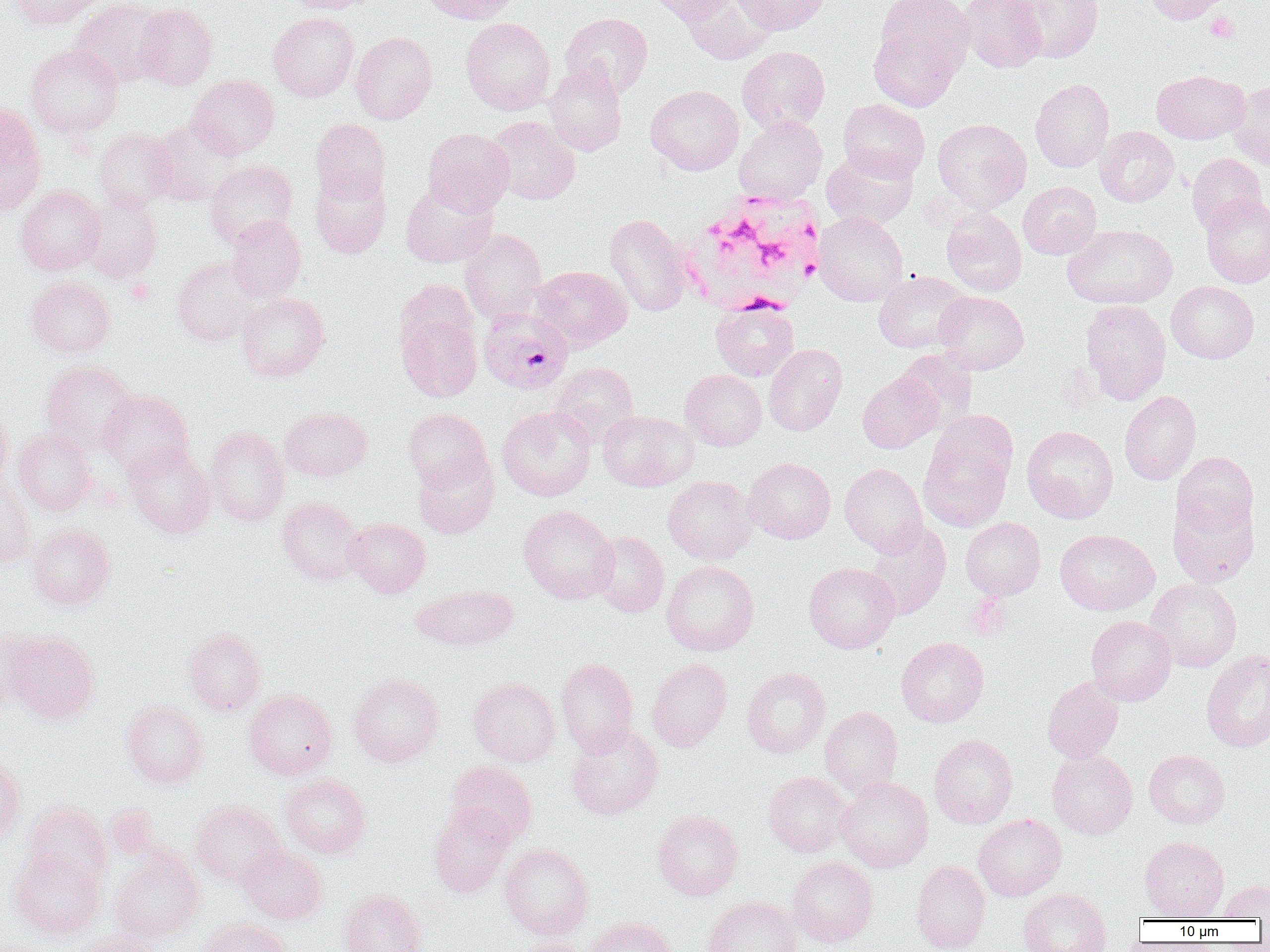

Approximate bounding boxes as (x1, y1, x2, y2) in pixels. Plasmodium falciparum-infected red blood cell locations: (478, 308, 572, 394). Platelet locations: (1206, 11, 1239, 42), (127, 279, 156, 304). White blood cell locations: (679, 189, 824, 315). Uninfected red blood cell locations: (9, 0, 105, 29), (71, 0, 168, 88), (284, 0, 381, 13), (419, 0, 521, 24), (643, 0, 736, 24), (682, 0, 778, 64), (734, 0, 831, 35), (874, 0, 973, 75), (958, 0, 1047, 73), (1007, 0, 1104, 63), (1143, 0, 1234, 24), (134, 4, 218, 91), (268, 12, 358, 102), (561, 13, 652, 98), (460, 17, 556, 115), (869, 24, 963, 111), (351, 31, 437, 124), (26, 44, 123, 138), (738, 46, 830, 134), (544, 63, 627, 156), (1152, 70, 1249, 144), (187, 74, 279, 159), (1030, 78, 1114, 171), (1229, 81, 1270, 170), (645, 85, 744, 175), (838, 99, 930, 182), (0, 102, 47, 215), (734, 115, 828, 203), (486, 116, 580, 205), (310, 118, 391, 204), (932, 118, 1031, 212), (147, 120, 240, 207), (1095, 126, 1179, 207), (94, 128, 177, 212), (423, 128, 514, 216), (822, 147, 918, 229), (1186, 153, 1266, 235), (205, 160, 298, 248), (310, 168, 391, 259), (1018, 181, 1101, 259), (400, 182, 498, 267), (15, 185, 105, 275), (1200, 193, 1270, 287), (82, 196, 163, 284), (941, 208, 1027, 296), (813, 211, 907, 306), (605, 213, 691, 316), (226, 215, 306, 301), (1062, 224, 1178, 309), (460, 228, 547, 323), (173, 256, 260, 346), (530, 265, 632, 352), (873, 270, 971, 353), (26, 277, 115, 357), (395, 279, 479, 358), (1166, 281, 1259, 363), (934, 290, 1029, 374), (236, 292, 330, 381), (1080, 299, 1171, 404), (710, 301, 798, 381), (396, 306, 482, 401), (763, 344, 847, 436), (895, 350, 978, 434), (41, 360, 138, 454), (550, 362, 638, 445), (680, 369, 767, 451), (857, 372, 943, 453), (99, 390, 193, 476), (1119, 390, 1201, 485), (497, 405, 596, 501), (0, 406, 13, 490), (279, 406, 372, 481), (403, 408, 491, 491), (598, 410, 697, 491), (205, 425, 289, 526), (1021, 425, 1118, 522), (14, 428, 96, 516), (918, 431, 1013, 531), (123, 442, 216, 538), (1171, 451, 1259, 538), (413, 452, 499, 538), (743, 457, 835, 543), (839, 463, 928, 554), (663, 476, 757, 565), (0, 479, 35, 569), (1169, 495, 1259, 587), (277, 497, 365, 585), (518, 504, 619, 604), (344, 517, 430, 598), (960, 517, 1045, 600), (864, 521, 951, 620), (28, 522, 115, 610), (1055, 529, 1159, 615), (589, 530, 669, 617), (661, 560, 759, 655), (803, 562, 899, 653), (1146, 578, 1242, 671), (412, 584, 519, 650), (1086, 616, 1176, 705), (0, 626, 38, 712), (183, 626, 266, 716), (3, 631, 100, 723), (896, 637, 989, 726), (1201, 650, 1270, 752), (556, 658, 639, 756), (646, 658, 732, 751), (741, 667, 830, 758), (349, 673, 444, 766), (1042, 676, 1124, 763), (469, 677, 560, 766), (244, 689, 337, 779), (121, 700, 209, 788), (820, 706, 903, 797), (566, 723, 663, 820), (929, 734, 1018, 828), (1047, 749, 1138, 839), (1144, 749, 1230, 827), (0, 757, 25, 844), (446, 760, 537, 846), (763, 771, 851, 857), (281, 774, 371, 858), (835, 776, 933, 872), (190, 800, 286, 887), (23, 802, 112, 890), (428, 803, 514, 897), (104, 804, 162, 861), (652, 809, 743, 900), (973, 813, 1067, 901), (1139, 835, 1229, 919), (500, 843, 593, 940), (239, 845, 327, 924), (9, 848, 105, 939), (110, 848, 204, 942), (787, 856, 878, 946), (911, 860, 990, 952), (1217, 879, 1270, 919), (1018, 887, 1111, 952), (338, 889, 427, 952), (703, 895, 800, 952), (587, 917, 678, 952), (197, 918, 290, 952), (74, 933, 168, 952), (512, 938, 591, 952). Slide-level diagnosis: Plasmodium falciparum. Captured at 1000x magnification. Single field of view. Thin blood smear. Image is 1270×952 pixels. Optical microscopy.